Assess this cell for malaria.
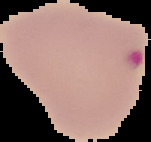
It is parasitized.

Summary:
  - Preparation: thin blood film
  - Image type: cell region segmented out of the field of view; surrounding area masked to black
  - Image size: 151×142 pixels